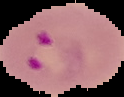

image_type: segmented cell region on a black background
image_size: 124×97 pixels
malaria_status: parasitized
preparation: thin blood smear